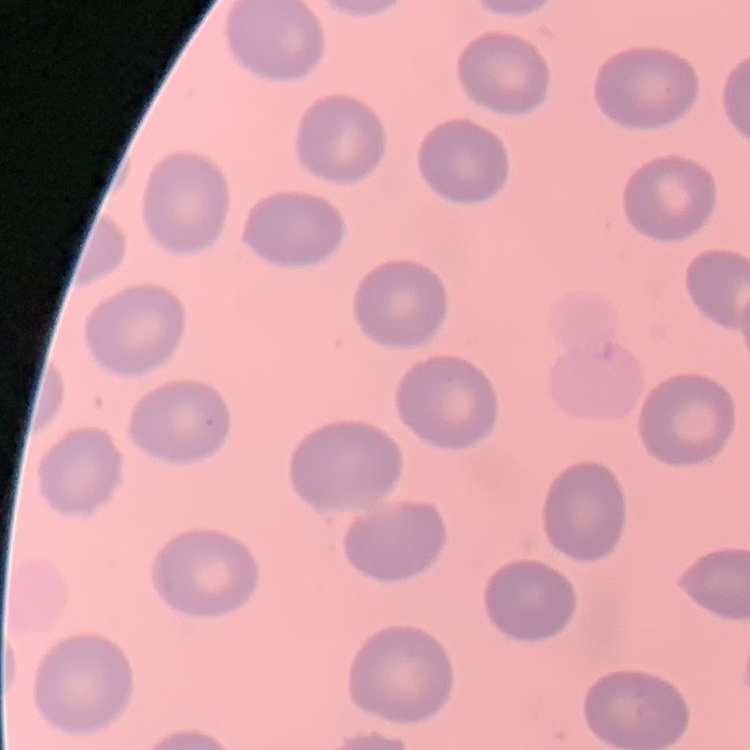
The red blood cells exhibit no rouleaux formation. Stained with either Field's or Giemsa. Thin blood smear. One tile cut from a larger photomicrograph.